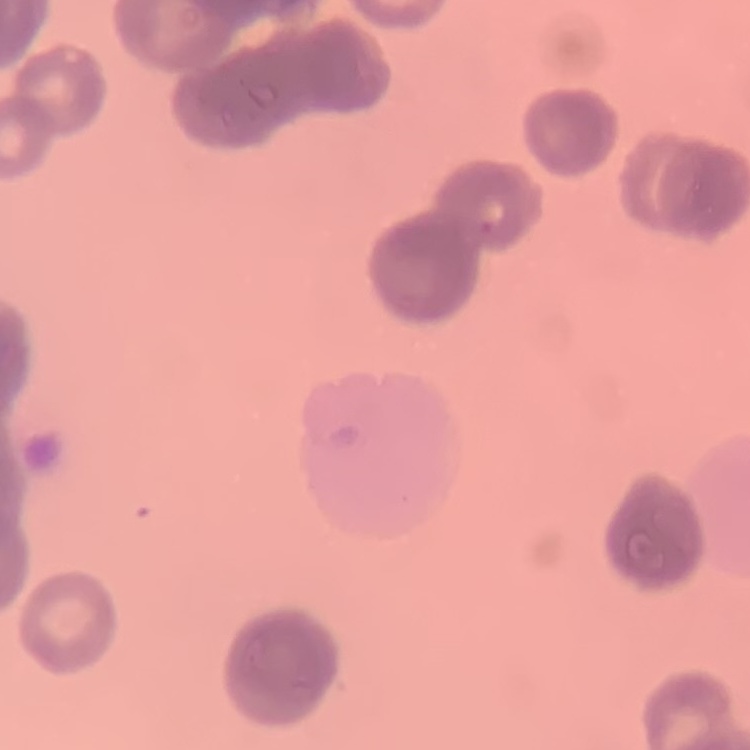

Summary:
  - Red blood cell morphology: rouleaux formation
  - Preparation: thin blood smear
  - Stain: Field's or Giemsa
  - Image type: square crop of a larger photomicrograph